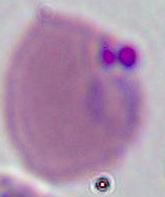 Captured at either 400x or 1000x magnification. Micrograph. A Plasmodium parasite is shown.